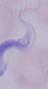
modality = micrograph
magnification = 1000x
identification = trypanosome